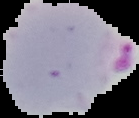
Summary:
  - Preparation: thin blood film
  - Image size: 139×118 pixels
  - Malaria status: parasitized
  - Image type: segmented cell region with the area outside set to black